Report the malaria status of this cell.
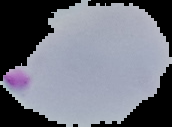

It is parasitized.

Summary:
  - Image type: segmented cell region with the area outside set to black
  - Preparation: thin blood film
  - Image size: 172×127 pixels